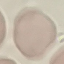
result: negative for malaria parasites
stain: Giemsa
preparation: thin smear
capture: smartphone through the microscope eyepiece
image_type: cell patch, automatically extracted from a larger field of view and resized to 64 × 64 pixels